Assess the morphology of the erythrocytes.
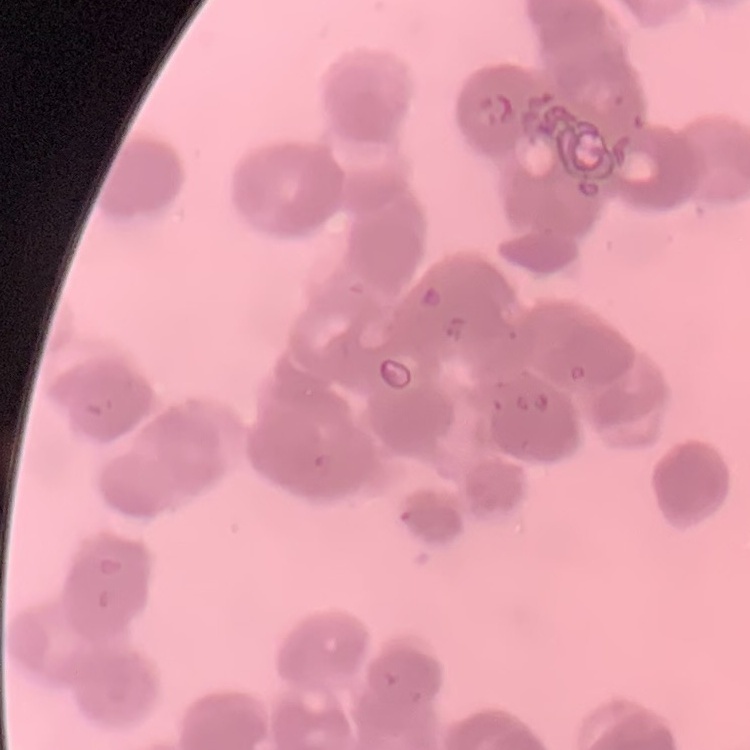
They show rouleaux formation.

Summary:
  - Preparation: thin peripheral smear
  - Stain: Field's or Giemsa
  - Image type: one tile cut from a larger photomicrograph